Assess the morphology of the erythrocytes.
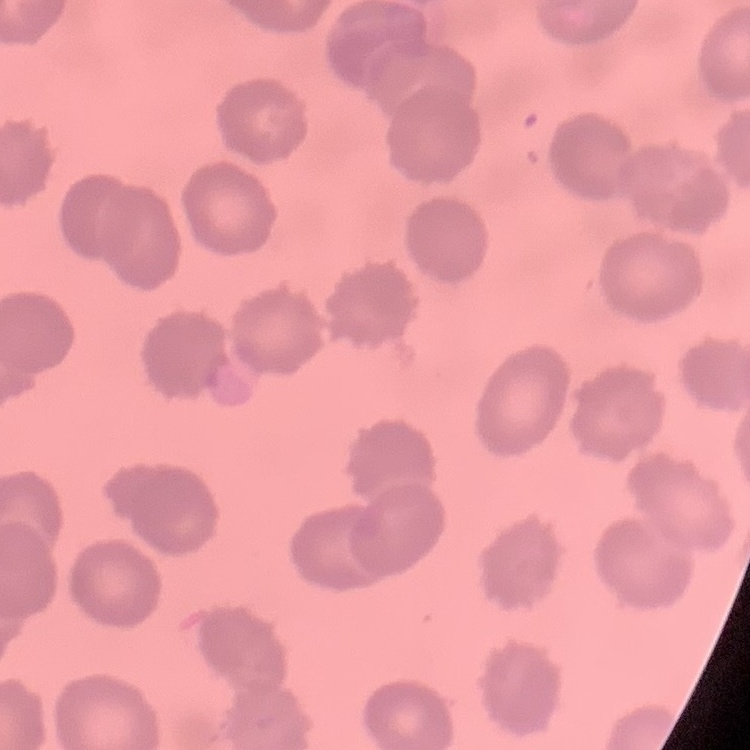
They show no rouleaux formation.

Field's or Giemsa stain. One tile cut from a larger photomicrograph. Thin blood smear.